State which parasite is depicted.
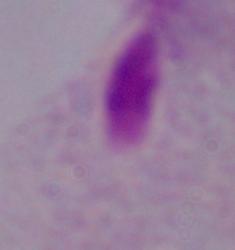

This is a trichomonad.

Photomicrograph. Captured at 1000x magnification.